Comment on the morphology of the red blood cells.
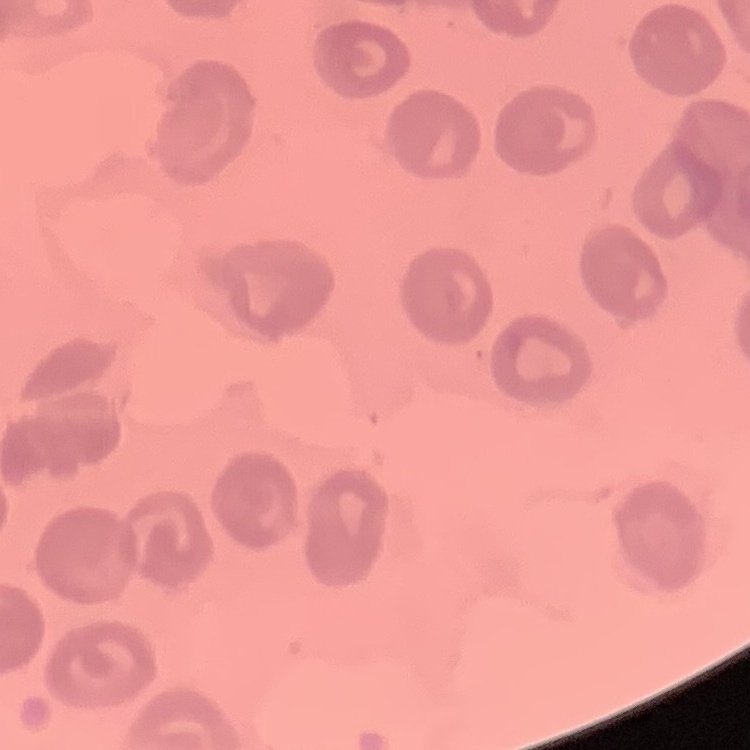
They show no rouleaux formation.

preparation: thin blood film
image_type: one tile cut from a larger photomicrograph
stain: Field's or Giemsa